Name the cell type shown.
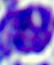

A leukocyte.

Summary:
  - Magnification: 400x
  - Modality: photomicrograph